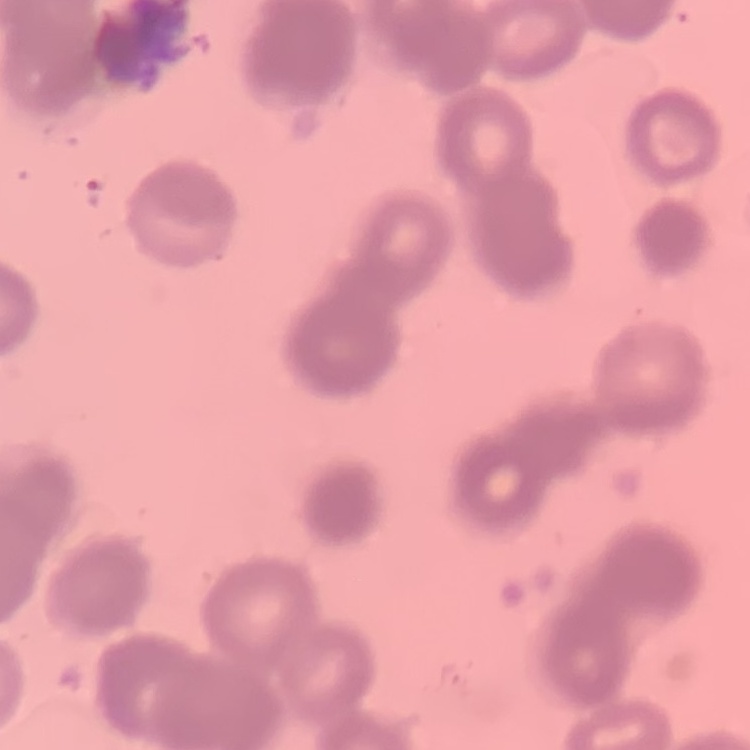
erythrocyte morphology = rouleaux formation
stain = Field's or Giemsa
preparation = thin blood smear
image type = square crop of a larger photomicrograph